Assess this cell for malaria.
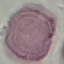

It is uninfected.

Summary:
  - Stain: Giemsa
  - Capture: smartphone camera at the microscope eyepiece
  - Preparation: thin smear
  - Image type: cell patch, automatically extracted from a larger field of view and resized to 64 × 64 pixels